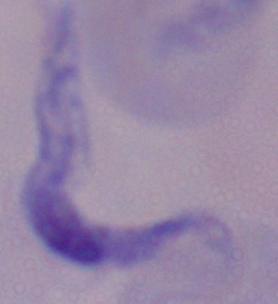

modality: photomicrograph
magnification: 1000x
identification: trypanosome